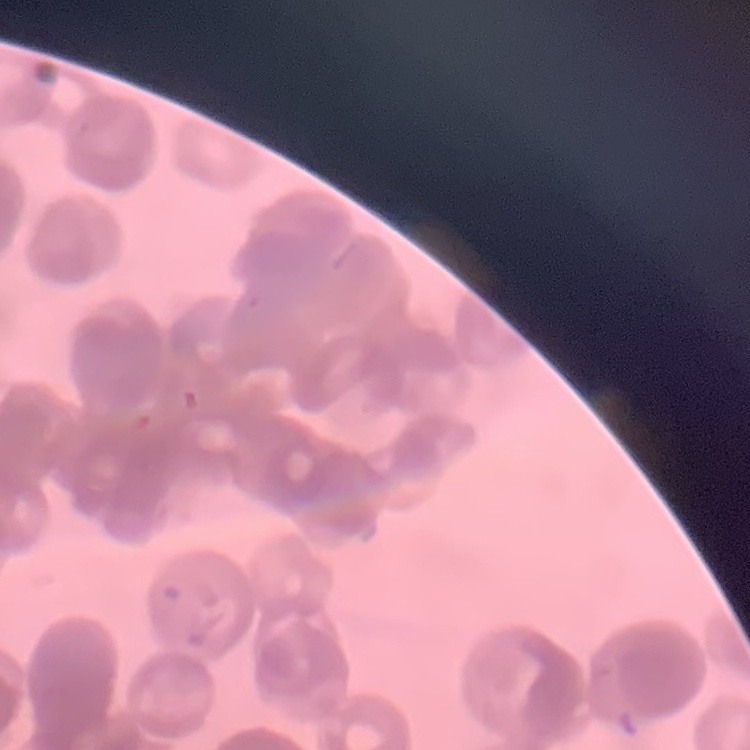
Summary:
  - Erythrocyte morphology: rouleaux formation
  - Stain: Field's or Giemsa
  - Preparation: thin blood film
  - Image type: one tile cut from a larger photomicrograph